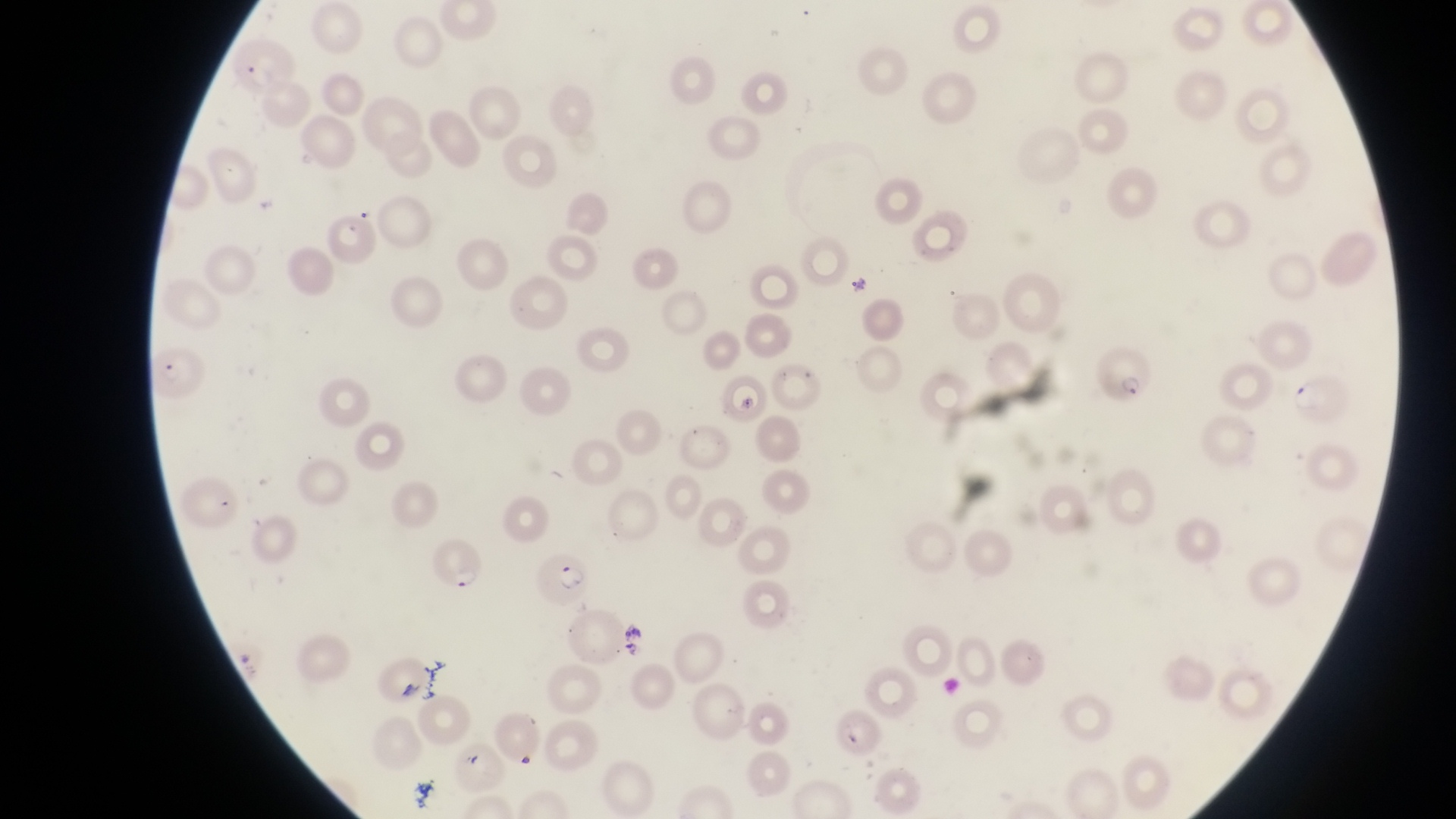

Approximate bounding boxes as (left, top, right, bottom) in pixels.
Summary:
  - Parasitised red blood cell locations: (222, 39, 296, 97), (146, 341, 207, 400), (1097, 343, 1156, 406), (1292, 373, 1353, 429), (426, 539, 487, 597), (535, 554, 593, 609)
  - Artifact (platelet-like body, stain precipitate, or debris) locations: (737, 391, 764, 425)
  - Image size: 1456×819 pixels
  - Preparation: thin blood smear
  - Country: Uganda
  - Field of view: single
  - Capture: smartphone photograph through the eyepiece of an Olympus CX-23 microscope
  - Magnification: 1000x